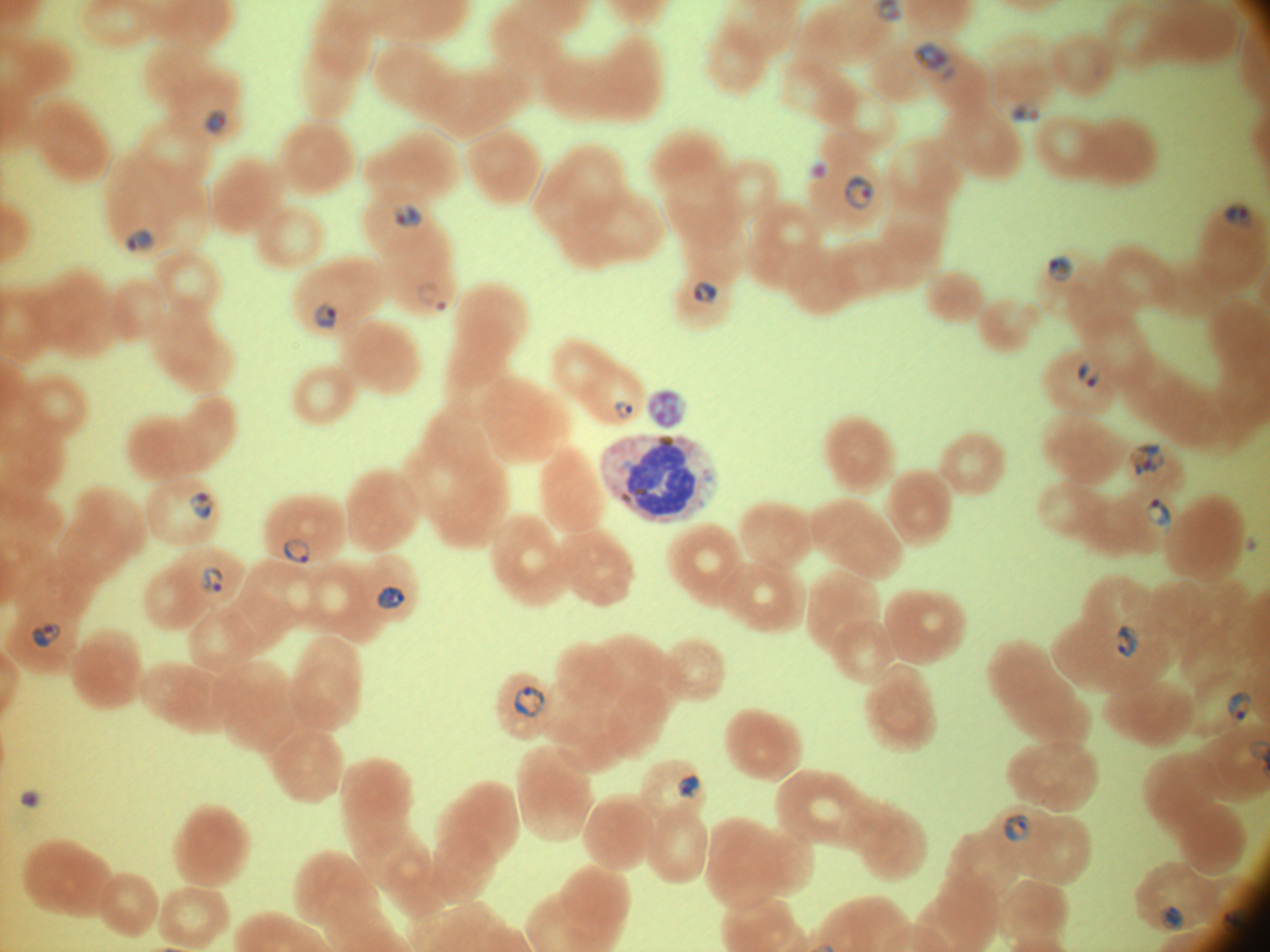
magnification = 100x
species = Plasmodium falciparum
field of view = one from this slide
image size = 1270×952 pixels
preparation = thin blood smear
stain = Giemsa
ring form locations = approximate bounding boxes as named x1/y1/x2/y2 corners in pixels, from the source annotation, which is not necessarily exhaustive: (x1=913, y1=41, x2=959, y2=84), (x1=1009, y1=104, x2=1041, y2=123), (x1=203, y1=107, x2=227, y2=134), (x1=811, y1=162, x2=829, y2=178), (x1=843, y1=174, x2=876, y2=211), (x1=394, y1=202, x2=424, y2=229), (x1=1225, y1=205, x2=1254, y2=227), (x1=125, y1=228, x2=155, y2=255), (x1=1046, y1=255, x2=1074, y2=283), (x1=693, y1=281, x2=719, y2=306), (x1=436, y1=301, x2=447, y2=312), (x1=312, y1=303, x2=340, y2=331), (x1=1077, y1=363, x2=1090, y2=380), (x1=1086, y1=371, x2=1101, y2=387), (x1=613, y1=400, x2=635, y2=421), (x1=1130, y1=443, x2=1166, y2=476), (x1=188, y1=490, x2=214, y2=520), (x1=1145, y1=498, x2=1172, y2=535), (x1=282, y1=537, x2=310, y2=563), (x1=199, y1=566, x2=224, y2=595), (x1=376, y1=586, x2=405, y2=609), (x1=30, y1=621, x2=62, y2=649), (x1=1116, y1=623, x2=1140, y2=658), (x1=513, y1=686, x2=546, y2=718), (x1=1226, y1=690, x2=1252, y2=721), (x1=676, y1=775, x2=702, y2=801), (x1=1002, y1=814, x2=1031, y2=843), (x1=1159, y1=904, x2=1185, y2=932), (x1=1221, y1=909, x2=1248, y2=934)
microscope = Leica DM2000 with built-in camera